State which cell type is depicted.
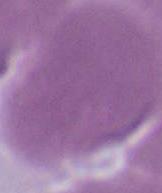

An erythrocyte.

{
  "modality": "micrograph",
  "magnification": "1000x"
}